State which parasite is depicted.
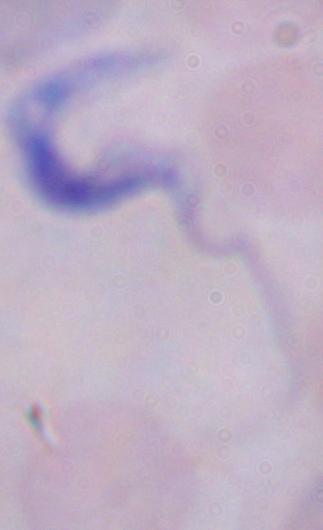

This is a trypanosome.

Photomicrograph. Captured at 1000x magnification.